Report the malaria status of this cell.
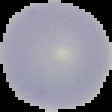

Uninfected.

From a thin blood film. Image is 112×112 pixels. Cell region segmented out of the field of view; the surrounding area is masked to black.